Classify this cell by malaria status.
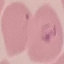

Parasitized.

Automatically extracted cell patch, resized to 64 × 64 pixels. Giemsa stain. Thin smear of blood. Acquired by smartphone through the microscope eyepiece.